Report the malaria status of this cell.
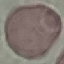

Uninfected.

Summary:
  - Preparation: thin blood film
  - Image type: automatically extracted cell patch, resized to 64 × 64 pixels
  - Stain: Giemsa
  - Capture: smartphone camera at the microscope eyepiece